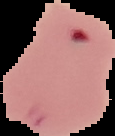

image size = 115×136 pixels
preparation = thin blood smear
image type = segmented cell region on a black background
result = malaria parasites identified